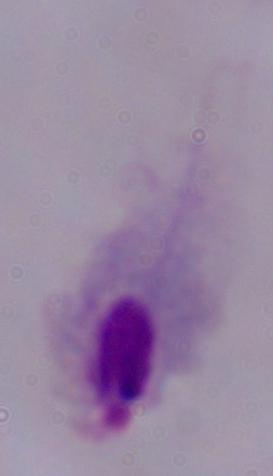

1000x magnification. Micrograph. A trichomonad is shown.